Give the position of every malaria parasite.
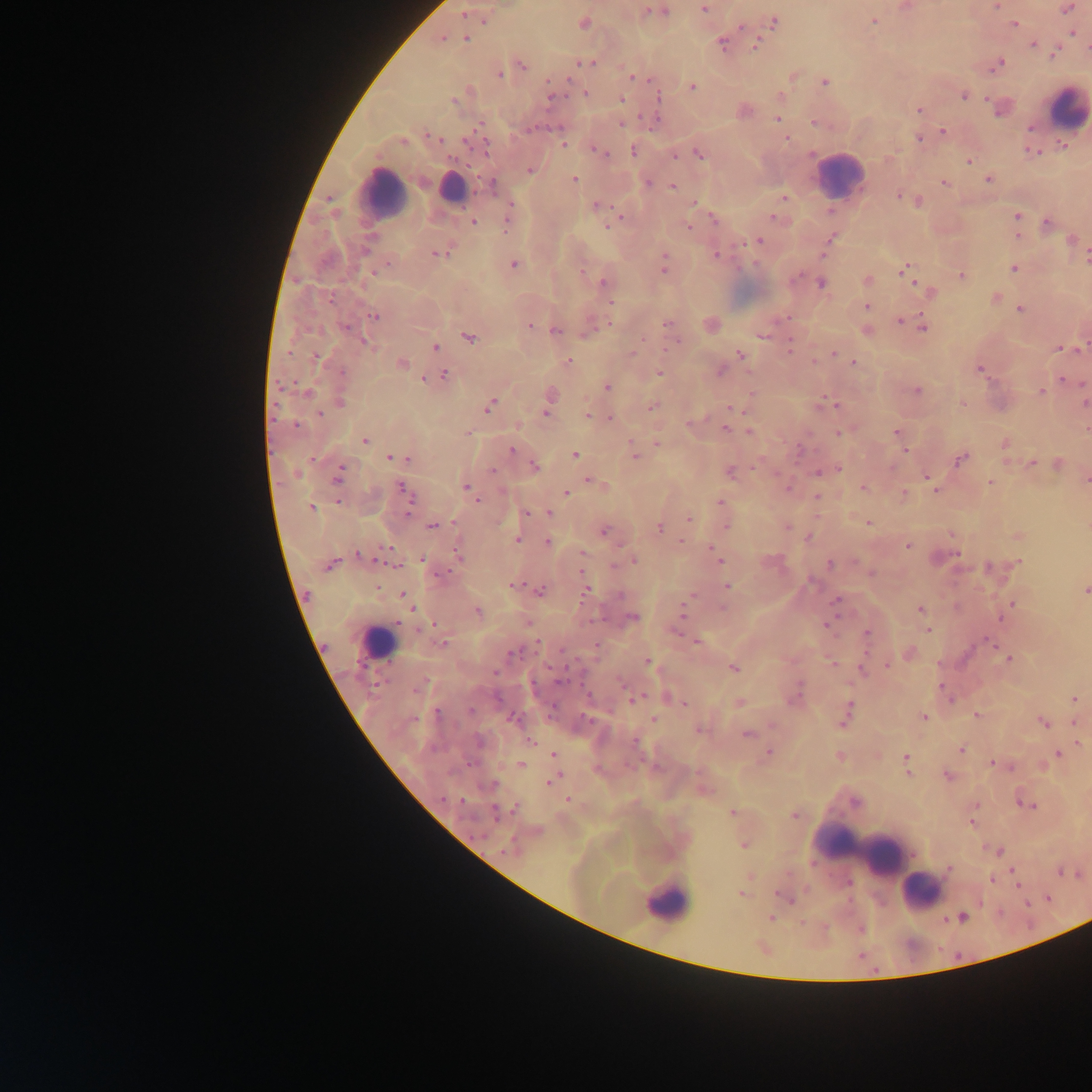

Approximate centers as [x, y] in pixels.
Malaria parasites: [905, 7], [997, 7], [704, 9], [1066, 9], [647, 10], [654, 11], [465, 14], [485, 17], [874, 21], [583, 22], [773, 22], [1014, 24], [1070, 27], [1073, 32], [440, 38], [465, 38], [722, 43], [756, 43], [1034, 44], [1056, 51], [584, 63], [997, 63], [520, 65], [500, 73], [633, 76], [792, 76], [823, 82], [692, 86], [586, 93], [962, 94], [550, 97], [656, 97], [780, 97], [456, 98], [621, 99], [1001, 107], [919, 110], [778, 118], [815, 122], [621, 124], [943, 131], [787, 138], [920, 138], [563, 144], [597, 150], [634, 150], [1031, 150], [673, 153], [698, 153], [968, 160], [530, 170], [574, 179], [988, 179], [944, 182], [648, 183], [492, 185], [672, 186], [899, 194], [784, 197], [918, 201], [694, 203], [597, 205], [1017, 216], [507, 218], [774, 218], [713, 219], [473, 222], [610, 223], [1047, 223], [688, 227], [1018, 234], [831, 238], [756, 240], [1071, 241], [438, 252], [716, 255], [1085, 258], [513, 263], [664, 265], [906, 268], [1014, 268], [961, 274], [866, 280], [604, 283], [821, 283], [930, 290], [994, 297], [610, 301], [867, 305], [1020, 309], [374, 315], [788, 318], [900, 320], [610, 323], [667, 323], [529, 325], [710, 325], [922, 326], [590, 329], [555, 330], [867, 331], [762, 335], [468, 336], [365, 343], [790, 345], [667, 347], [435, 348], [1061, 348], [631, 353], [834, 353], [740, 355], [568, 361], [814, 361], [401, 363], [853, 363], [978, 369], [719, 370], [659, 372], [443, 374], [1063, 379], [607, 386], [916, 390], [1040, 392], [550, 394], [339, 401], [1084, 402], [962, 403], [489, 405], [834, 405], [652, 407], [730, 408], [546, 411], [587, 415], [611, 418], [692, 423], [726, 429], [1086, 429], [750, 431], [839, 432], [896, 432], [365, 440], [657, 443], [1004, 444], [512, 449], [905, 451], [633, 453], [574, 454], [394, 458], [402, 458], [960, 458], [1031, 463], [1058, 464], [533, 465], [837, 469], [827, 470], [729, 471], [819, 471], [338, 475], [925, 476], [1085, 479], [591, 481], [990, 482], [600, 484], [466, 487], [788, 488], [863, 488], [935, 489], [403, 491], [566, 493], [903, 494], [817, 496], [474, 499], [720, 502], [311, 508], [526, 513], [548, 513], [688, 520], [869, 523], [432, 525], [725, 526], [787, 526], [660, 527], [603, 531], [951, 534], [809, 536], [1018, 536], [518, 539], [547, 542], [907, 545], [713, 549], [458, 551], [633, 560], [718, 560], [1019, 562], [330, 564], [830, 564], [512, 585], [727, 586], [587, 589], [1085, 589], [539, 591], [403, 596], [836, 600], [1012, 603], [920, 609], [683, 611], [477, 612], [631, 617], [826, 625], [928, 629], [866, 634], [697, 641], [989, 641], [442, 643], [909, 653], [1009, 659], [648, 661], [832, 663], [887, 664], [733, 667], [861, 670], [797, 692], [634, 698], [668, 698], [1074, 698], [683, 702], [739, 702], [846, 715], [977, 715], [923, 717], [513, 718], [653, 719], [1074, 721], [1043, 722], [699, 729], [747, 734], [530, 741], [1077, 743], [961, 750], [768, 752], [1058, 753], [554, 755], [840, 755], [906, 758], [991, 762], [520, 765], [908, 773], [948, 776], [553, 778], [703, 790], [567, 800], [1021, 801], [975, 805], [1030, 805], [732, 813], [794, 815], [971, 823], [743, 845], [997, 850], [948, 868], [1012, 871], [1059, 871], [991, 879], [742, 893], [787, 897], [771, 917], [962, 917], [761, 947].

Summary:
  - Leukocyte locations: [1065, 108], [839, 176], [451, 188], [381, 194], [377, 643], [869, 855], [921, 891], [666, 902]
  - Country: Ghana
  - Image size: 1092×1092 pixels
  - Field of view: single
  - Capture: mobile-phone photograph through a microscope
  - Preparation: thick blood film